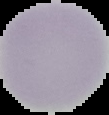

preparation = thin blood smear
image size = 109×115 pixels
malaria status = uninfected
image type = segmented cell region on a black background